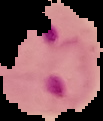 From a thin blood smear. The area outside the segmented cell region is set to black. Image is 103×121 pixels. Result: malaria parasites identified.